State the blood parasite species.
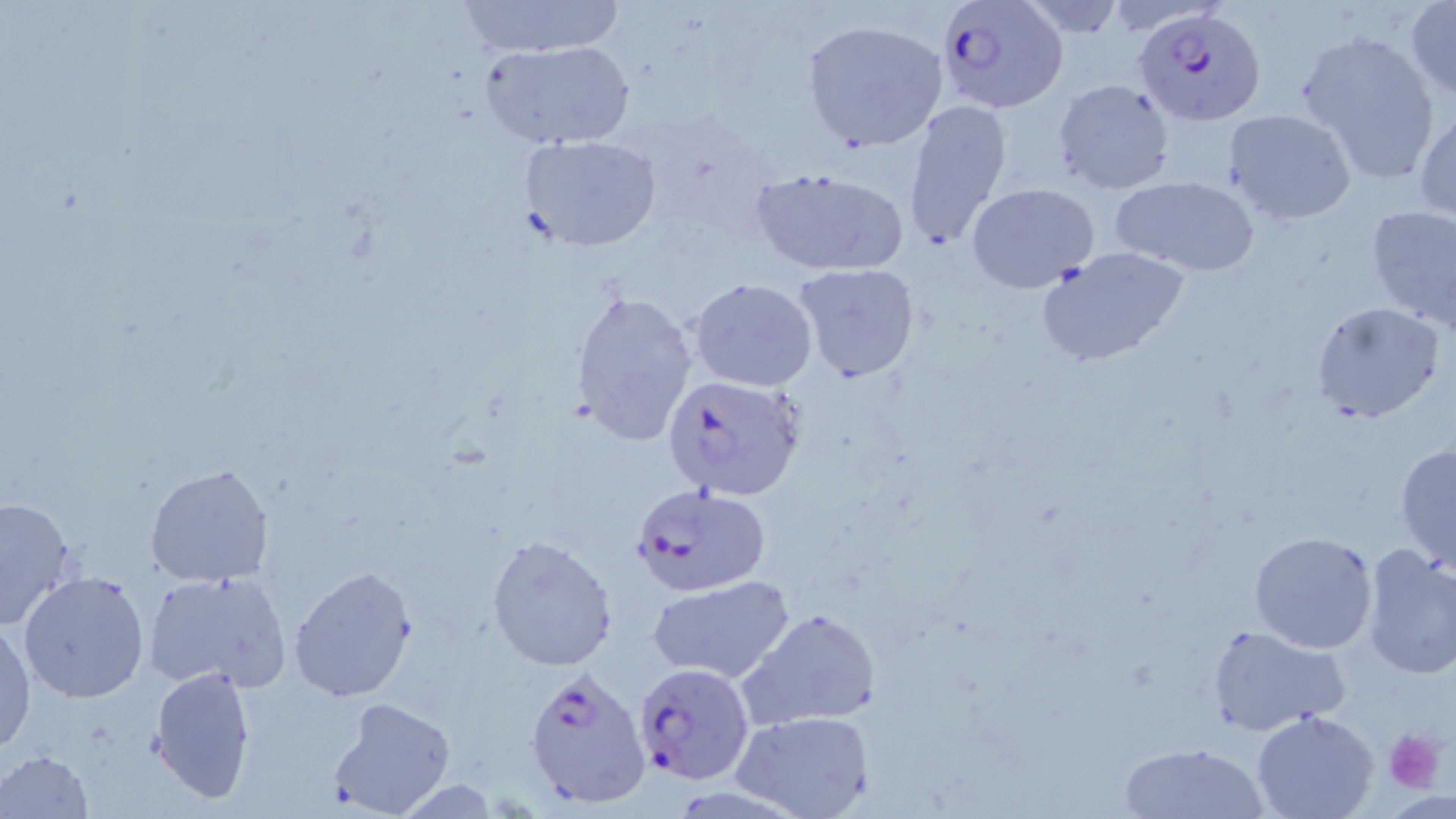

Plasmodium falciparum.

Approximate bounding boxes as (x1, y1, x2, y2) in pixels. Plasmodium falciparum-infected red blood cell locations: (938, 0, 1067, 112), (1134, 4, 1265, 124), (660, 372, 807, 500), (626, 484, 775, 599), (632, 663, 757, 787), (523, 665, 653, 807). Platelet locations: (1383, 728, 1446, 794). Uninfected red blood cell locations: (455, 1, 627, 57), (1405, 1, 1456, 101), (802, 19, 948, 151), (1296, 31, 1439, 181), (479, 38, 636, 150), (1052, 78, 1175, 195), (902, 99, 1014, 249), (1414, 106, 1456, 222), (1224, 109, 1356, 226), (517, 134, 662, 252), (748, 166, 907, 276), (1110, 175, 1260, 276), (967, 184, 1099, 294), (1364, 205, 1456, 329), (1034, 246, 1192, 370), (793, 264, 922, 385), (687, 277, 817, 391), (570, 287, 699, 447), (1309, 302, 1443, 425), (1394, 444, 1456, 573), (144, 462, 274, 586), (0, 495, 79, 631), (1247, 530, 1379, 654), (486, 534, 620, 670), (1358, 545, 1456, 681), (287, 564, 418, 702), (18, 570, 150, 704), (141, 570, 294, 694), (644, 577, 794, 683), (739, 608, 881, 730), (0, 620, 36, 755), (1205, 622, 1351, 738), (149, 663, 257, 805), (329, 697, 457, 817), (731, 709, 877, 819), (1250, 710, 1380, 819), (1119, 740, 1268, 818), (0, 749, 96, 818). Single field of view. 1000x magnification. Image is 1456×819 pixels. May-Grünwald-Giemsa stain. Optical microscopy. Thin blood film.